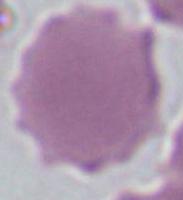 Micrograph. Captured at 1000x magnification. A red blood cell is shown.